Report the malaria status of this cell.
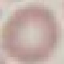
Uninfected.

Thin blood film. Giemsa-stained preparation. Automatically extracted cell patch, resized to 64 × 64 pixels. Photographed with a smartphone camera at the microscope eyepiece.